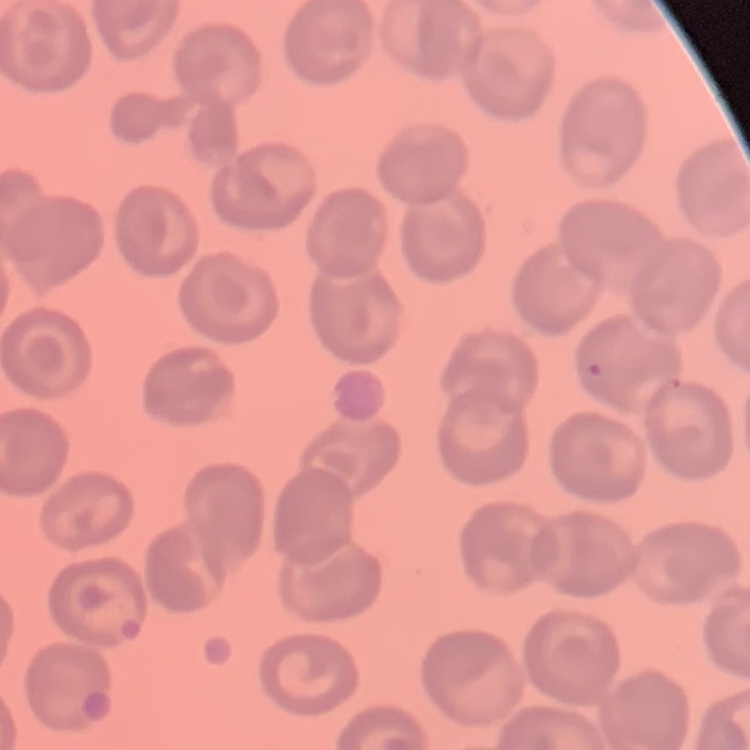

The red blood cells exhibit no rouleaux formation. Stained with either Field's or Giemsa. Thin blood smear. One tile cut from a larger photomicrograph.